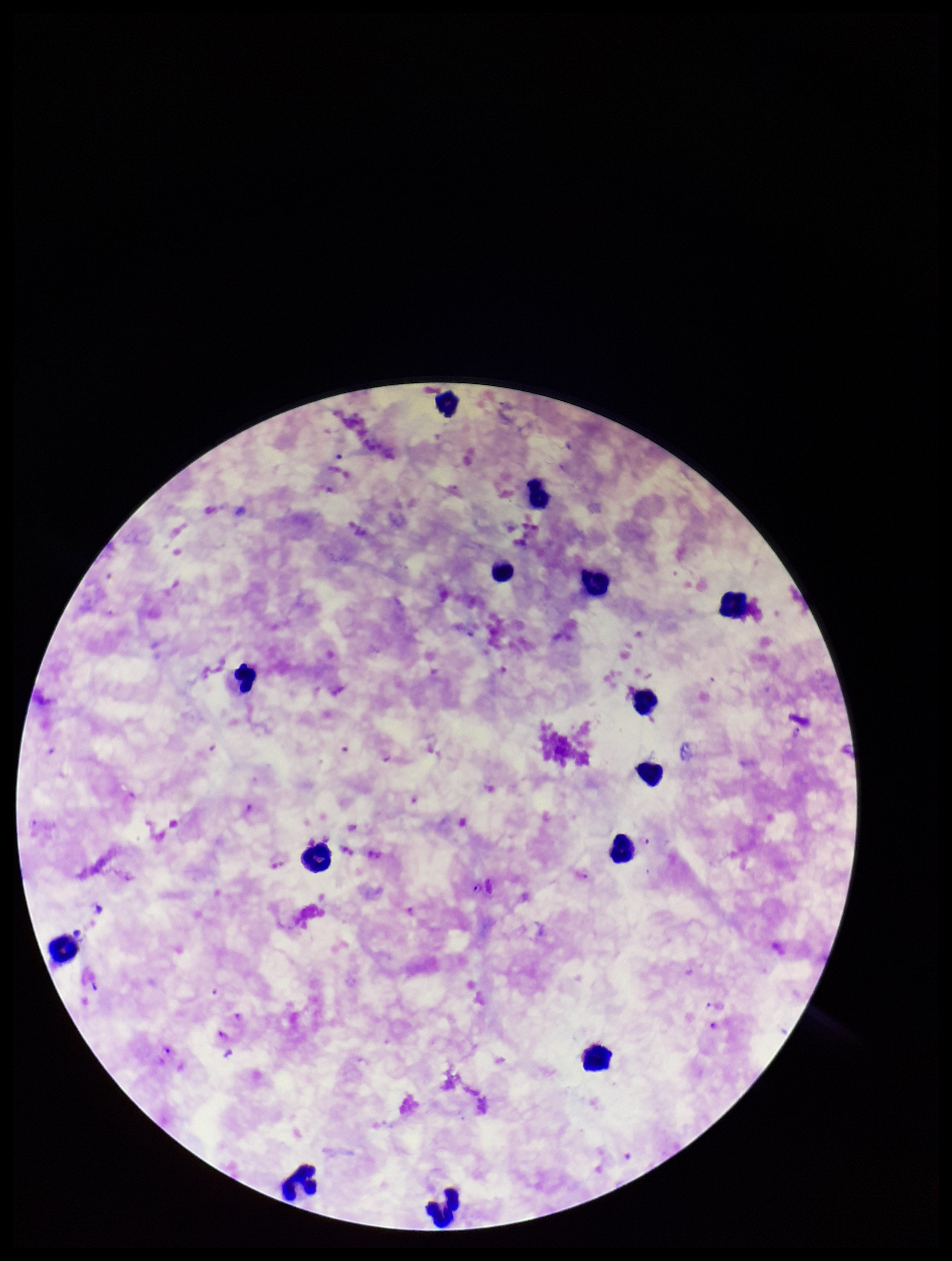
Summary:
  - Leukocyte count: 14
  - Image size: 952×1261 pixels
  - Parasite count: 5
  - Field of view: one from this slide
  - Capture: smartphone photograph through the microscope eyepiece
  - Stain: Giemsa
  - Patient malaria status: infected
  - Preparation: thick blood smear
  - Plasmodium parasites: detected
  - Species reported for this patient: Plasmodium falciparum